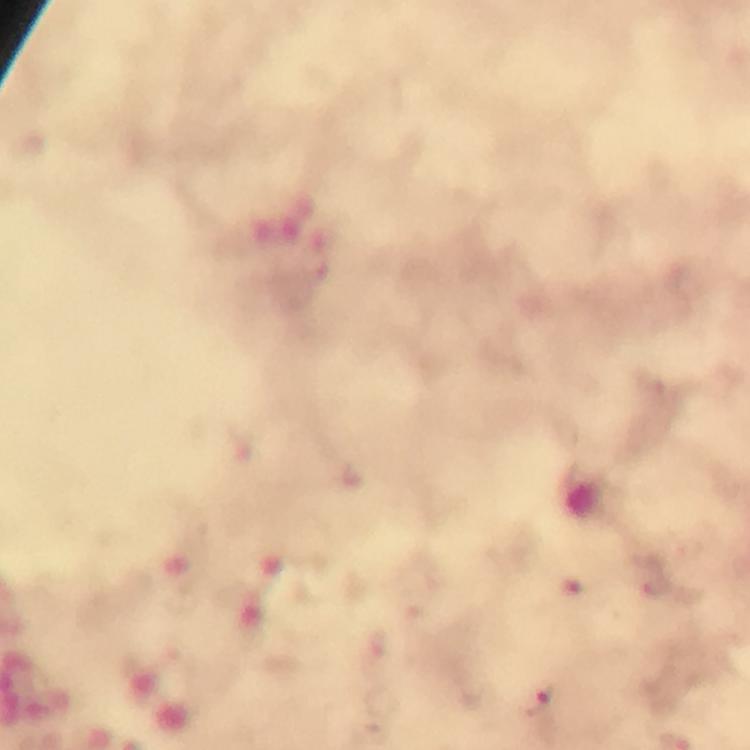
image_size: 750×750 pixels
stain: Giemsa
plasmodium_parasite_locations: 'approximate centers as [x, y] in pixels: [537, 703]'
magnification: 100x
immersion_oil: applied
capture: smartphone mounted on the microscope
context: from a malaria diagnostic workup
cropped_from: one field of view
preparation: thick smear